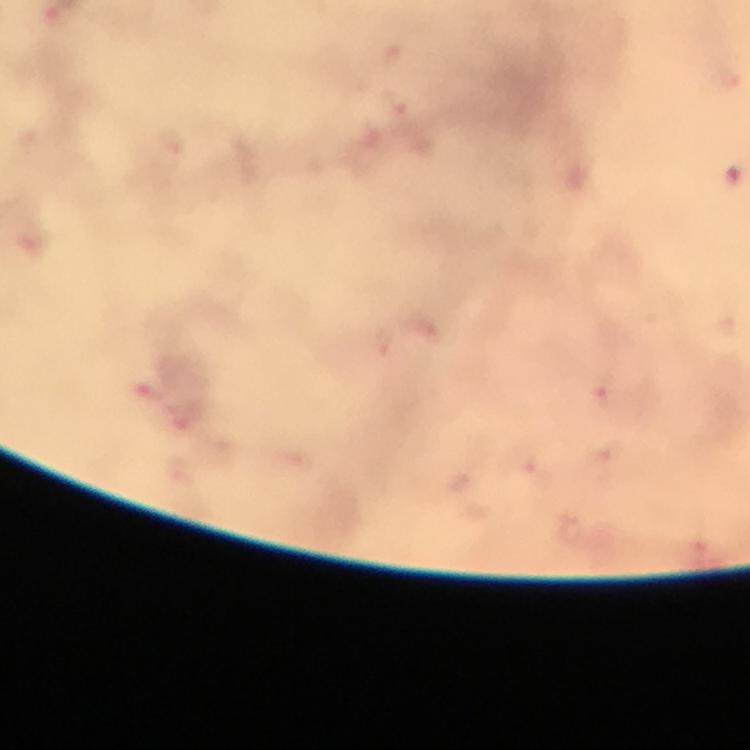
Approximate centers as (x, y) in pixels.
Summary:
  - Malaria parasite locations: (604, 394)
  - Cropped from: one field of view
  - Magnification: 100x
  - Preparation: thick blood smear
  - Immersion oil: applied
  - Context: from a malaria diagnostic workup
  - Image size: 750×750 pixels
  - Stain: Giemsa
  - Capture: smartphone camera through the microscope